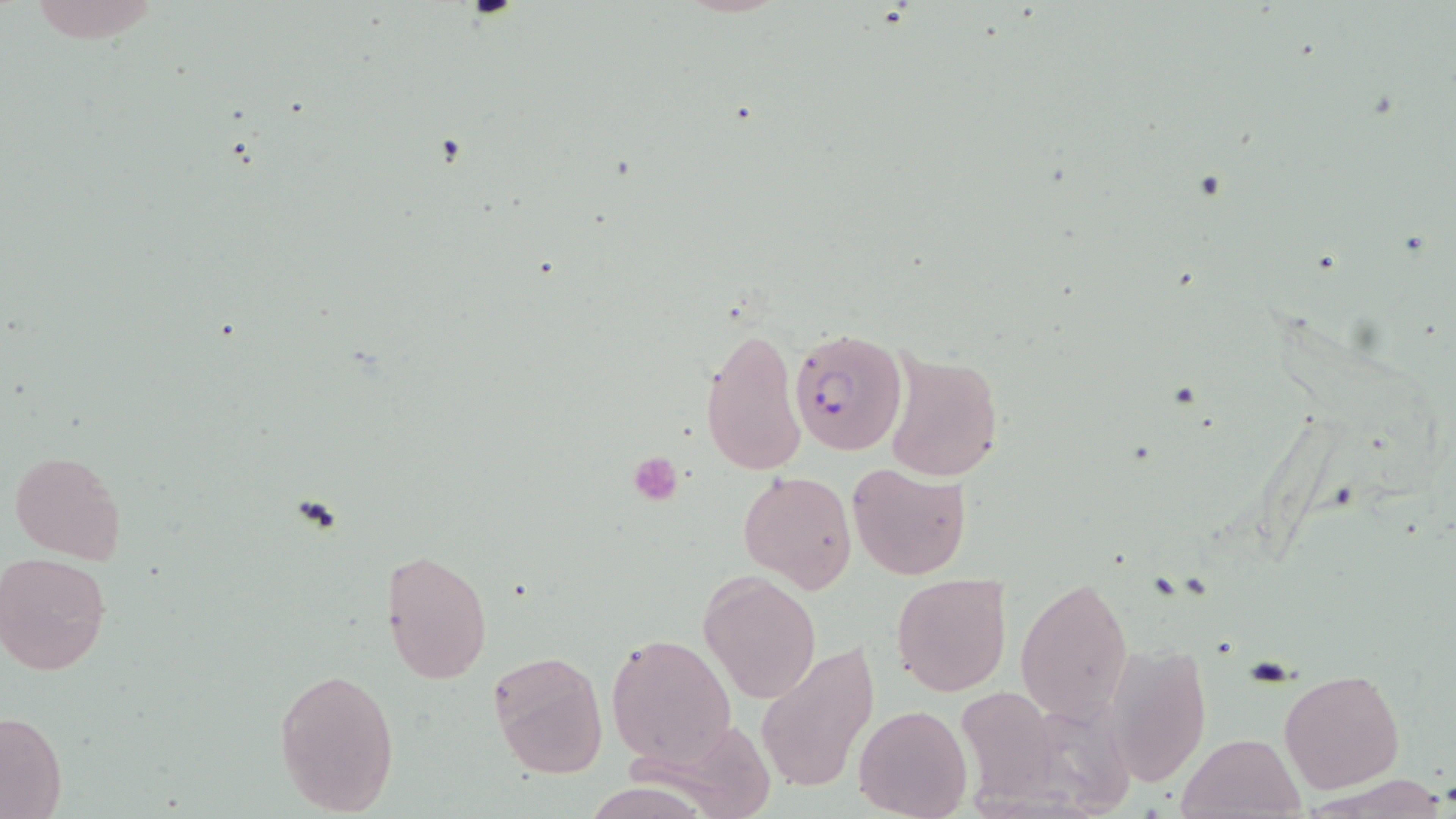
slide-level diagnosis = Plasmodium falciparum
modality = optical microscopy
magnification = 1000x
uninfected red blood cell locations = approximate bounding boxes as [x1, y1, x2, y2] in pixels: [699, 322, 807, 479], [882, 351, 1003, 482], [10, 450, 126, 566], [847, 461, 971, 582], [738, 469, 858, 591], [382, 547, 493, 688], [1, 552, 114, 677], [699, 572, 820, 704], [891, 572, 1013, 697], [1015, 578, 1134, 722], [605, 633, 736, 767], [1098, 641, 1212, 787], [756, 647, 875, 795], [488, 650, 609, 779], [273, 666, 400, 817], [1279, 668, 1404, 792], [954, 687, 1064, 798], [855, 703, 971, 818], [0, 710, 68, 818], [1177, 730, 1306, 819]
field of view = one of a larger specimen
preparation = thin blood film
stain = May-Grünwald-Giemsa
image size = 1456×819 pixels
Plasmodium falciparum-infected red blood cell locations = approximate bounding boxes as [x1, y1, x2, y2] in pixels: [789, 329, 907, 458]
platelet locations = approximate bounding boxes as [x1, y1, x2, y2] in pixels: [628, 453, 683, 507]